Locate every blood parasite and identify its species.
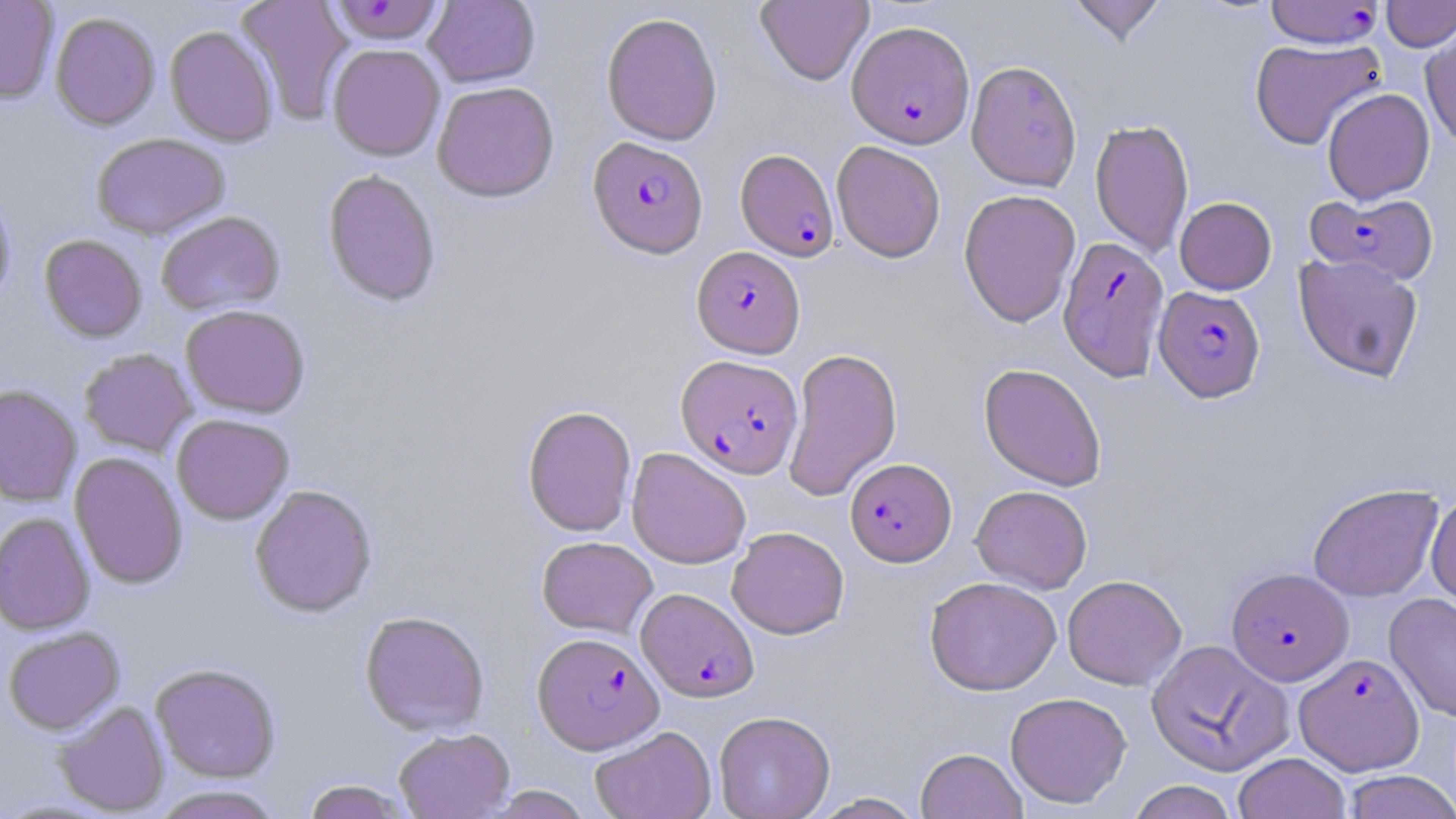
Approximate bounding boxes as [x1, y1, x2, y2] in pixels.
Plasmodium falciparum-infected red blood cells: [1265, 0, 1383, 48], [328, 1, 446, 46], [847, 21, 974, 148], [588, 136, 709, 258], [735, 148, 840, 261], [1305, 191, 1439, 286], [1058, 234, 1169, 380], [691, 246, 805, 358], [1154, 286, 1265, 402], [676, 354, 803, 478], [845, 458, 956, 566], [1226, 567, 1353, 685], [637, 587, 759, 703], [532, 631, 663, 753], [1295, 653, 1423, 775].
No Plasmodium ovale, Plasmodium malariae, Plasmodium vivax, Babesia divergens, or Trypanosoma brucei observed.

slide-level diagnosis = Plasmodium falciparum
field of view = one of a larger specimen
magnification = 1000x
image size = 1456×819 pixels
preparation = thin blood smear
stain = May-Grünwald-Giemsa
modality = light microscopy
uninfected red blood cell locations = approximate bounding boxes as [x1, y1, x2, y2] in pixels: [0, 0, 59, 105], [235, 0, 354, 125], [424, 0, 540, 88], [756, 0, 873, 86], [1066, 0, 1168, 46], [1382, 0, 1456, 51], [600, 11, 723, 146], [50, 12, 160, 131], [165, 25, 278, 148], [1421, 25, 1456, 151], [1250, 37, 1386, 150], [327, 44, 445, 162], [966, 60, 1082, 191], [432, 81, 560, 203], [1322, 88, 1435, 204], [1090, 118, 1193, 257], [91, 133, 230, 240], [831, 141, 946, 262], [322, 169, 441, 308], [958, 189, 1081, 327], [0, 191, 16, 310], [1174, 196, 1277, 294], [156, 211, 284, 316], [39, 234, 148, 343], [1293, 253, 1424, 381], [180, 305, 310, 418], [782, 346, 903, 501], [79, 348, 197, 458], [979, 362, 1107, 491], [0, 384, 82, 507], [522, 405, 637, 537], [171, 414, 294, 525], [627, 447, 751, 569], [69, 452, 188, 590], [1308, 483, 1443, 603], [249, 484, 377, 617], [971, 485, 1092, 594], [1426, 491, 1456, 610], [0, 512, 95, 635], [727, 526, 849, 639], [536, 536, 658, 638], [1062, 574, 1186, 690], [924, 576, 1062, 696], [1385, 593, 1456, 723], [359, 609, 490, 736], [2, 626, 125, 735], [1145, 639, 1292, 776], [150, 663, 281, 784], [1005, 692, 1131, 808], [53, 701, 170, 816], [714, 710, 835, 819], [590, 725, 716, 819], [393, 728, 515, 818], [916, 747, 1027, 819], [1232, 752, 1351, 819], [1341, 770, 1456, 818], [300, 779, 416, 819], [1126, 780, 1239, 819], [149, 785, 286, 819], [482, 785, 594, 818], [809, 792, 926, 818]